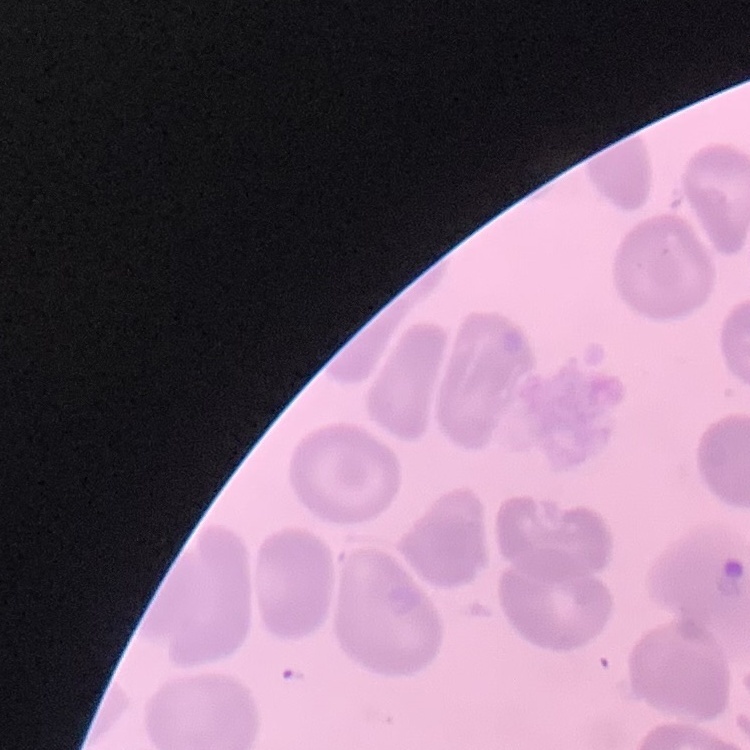

Summary:
  - Erythrocyte morphology: no rouleaux formation
  - Stain: Field's or Giemsa
  - Image type: one tile cut from a larger photomicrograph
  - Preparation: thin blood film